Comment on the morphology of the erythrocytes.
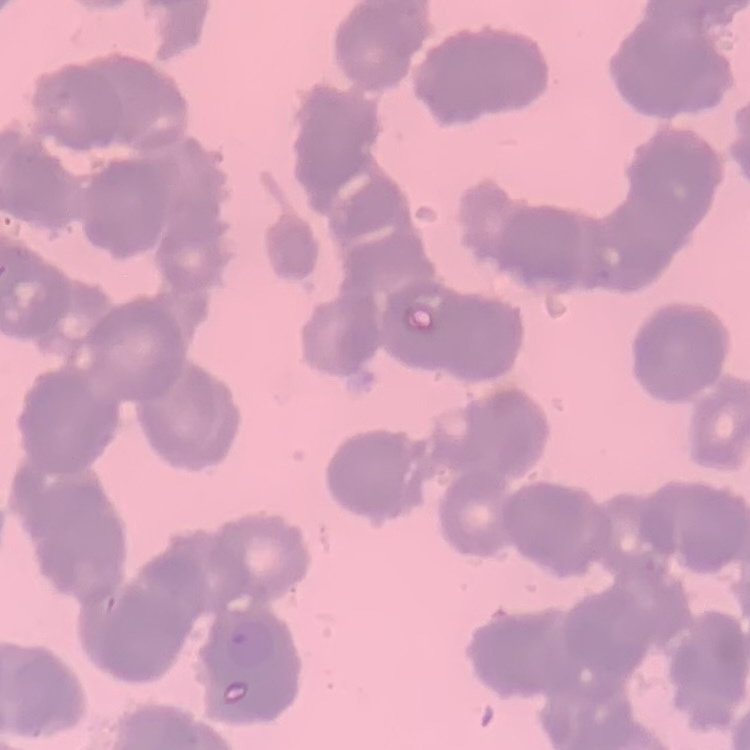
Rouleaux formation.

image_type: one tile cut from a larger photomicrograph
preparation: thin blood smear
stain: Field's or Giemsa